Assess this cell for malaria.
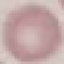

Uninfected.

Automatically extracted cell patch, resized to 64 × 64 pixels. Acquired by smartphone through the microscope eyepiece. Giemsa-stained preparation. Thin smear of blood.